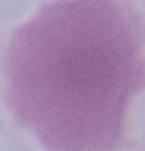

magnification: 1000x
modality: photomicrograph
identification: red blood cell